Describe the morphology of the erythrocytes.
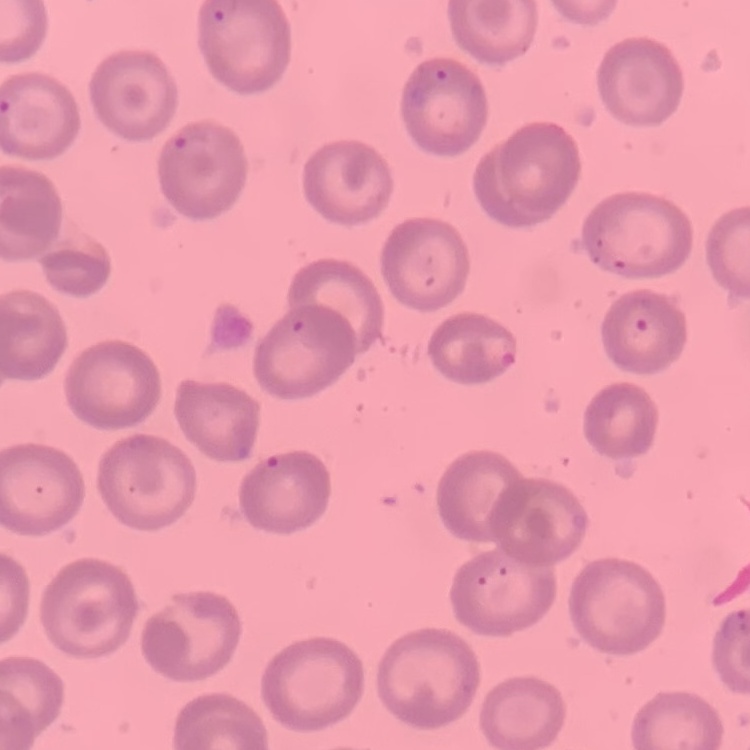

They show no rouleaux formation.

Field's or Giemsa stain. Thin blood smear. One tile cut from a larger photomicrograph.